Assess the morphology of the erythrocytes.
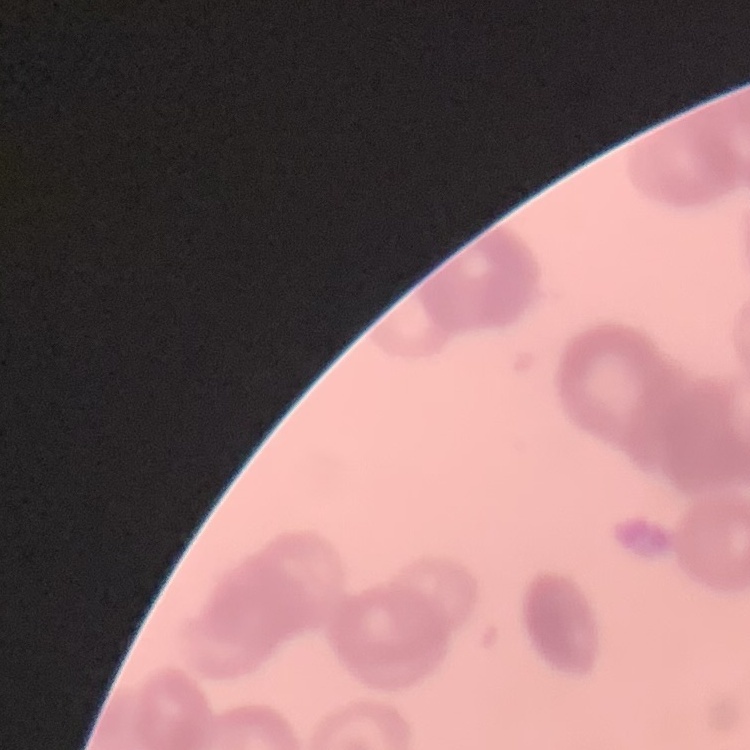

They show rouleaux formation.

preparation = thin peripheral smear
stain = Field's or Giemsa
image type = square crop of a larger photomicrograph